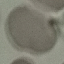 Malaria status: uninfected. Cell patch, automatically extracted from a larger field of view and resized to 64 × 64 pixels. Photographed with a smartphone camera at the microscope eyepiece. Giemsa stain. Thin smear of blood.